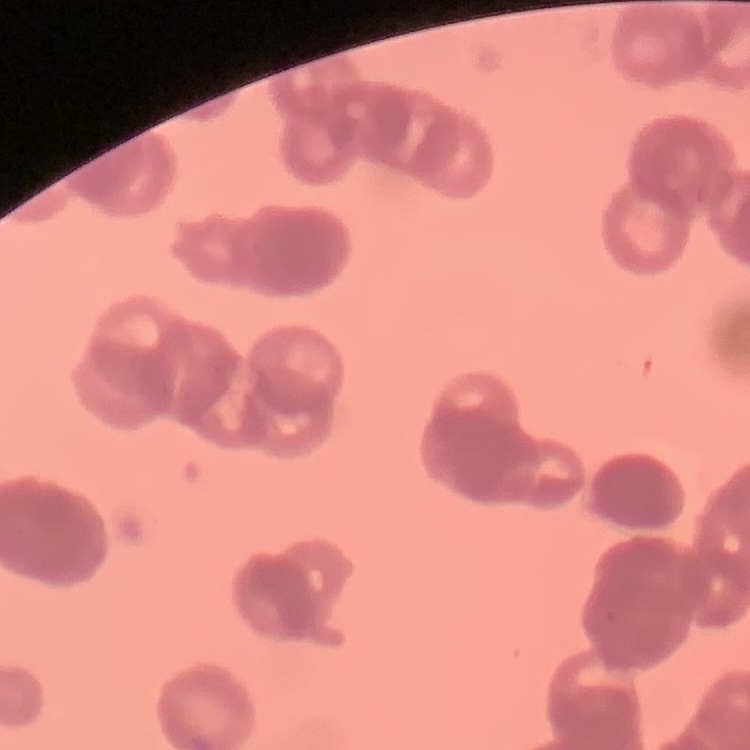

Summary:
  - Erythrocyte morphology: rouleaux formation
  - Image type: square crop of a larger photomicrograph
  - Preparation: thin blood smear
  - Stain: Field's or Giemsa